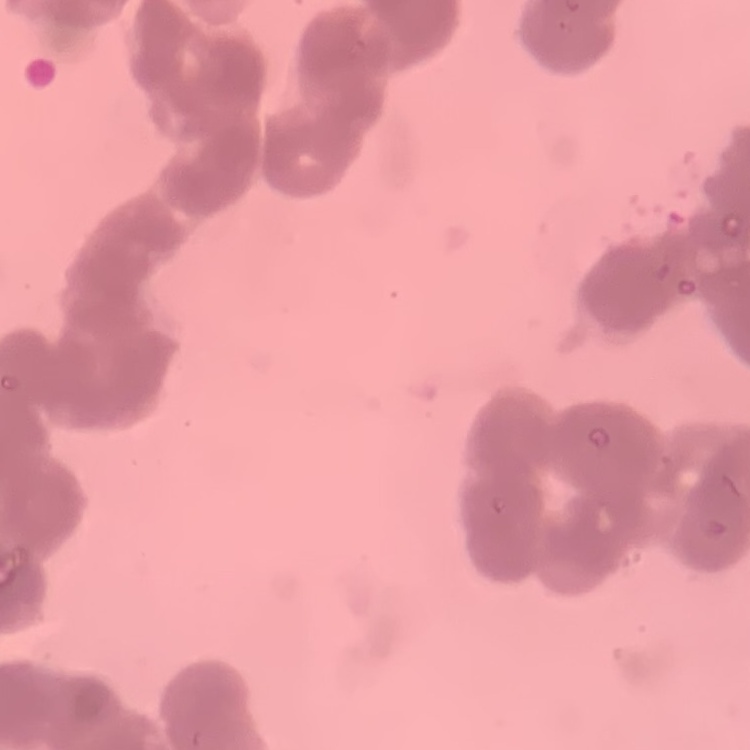

{
  "red_blood_cell_morphology": "rouleaux formation",
  "stain": "Field's or Giemsa",
  "preparation": "thin peripheral smear",
  "image_type": "one tile cut from a larger photomicrograph"
}